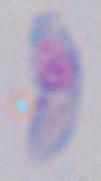

Summary:
  - Identification: Toxoplasma gondii
  - Modality: photomicrograph
  - Magnification: 1000x